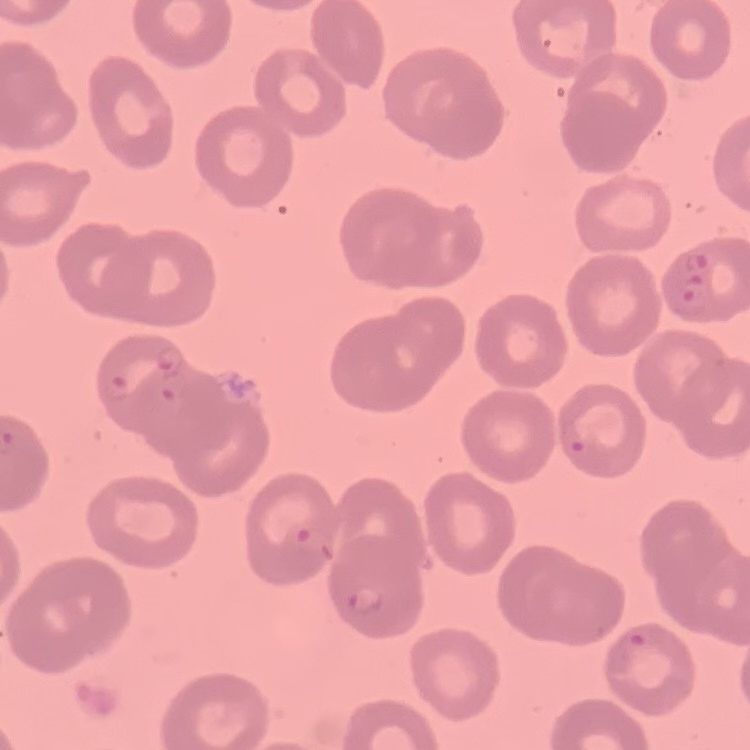

erythrocyte_morphology: no rouleaux formation
stain: Field's or Giemsa
preparation: thin blood film
image_type: square crop of a larger photomicrograph